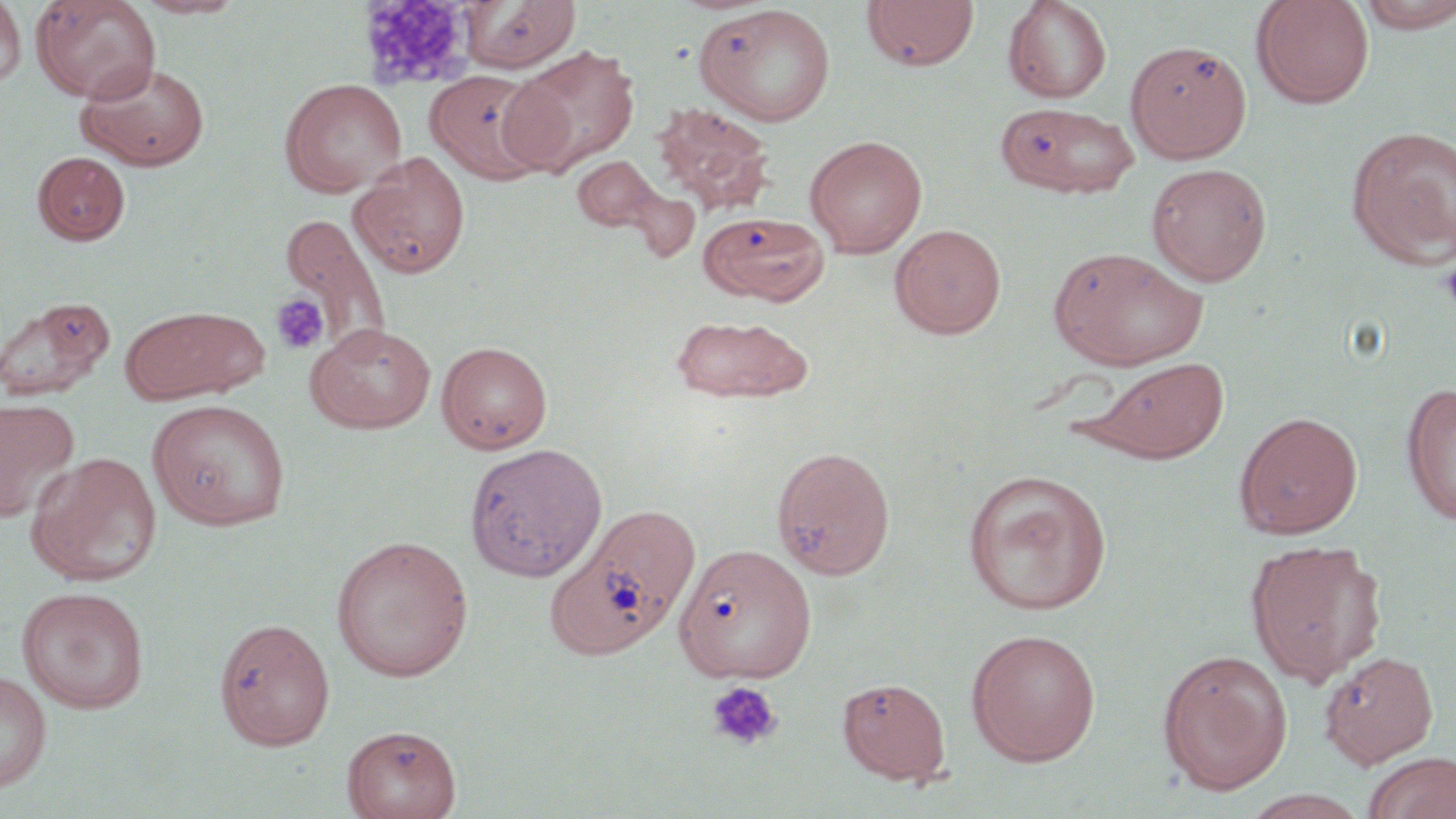

Summary:
  - Coordinate format: approximate bounding boxes as (x1,y1)-(x2,y2) corner pairs in pixels
  - Platelet locations: (1439,257)-(1456,313), (271,293)-(329,355), (706,681)-(783,750)
  - White blood cell locations: (355,1)-(482,92)
  - Uninfected red blood cell locations: (30,0)-(162,103), (133,0)-(247,19), (460,0)-(581,72), (861,0)-(980,72), (1003,0)-(1112,103), (1250,0)-(1376,109), (0,1)-(27,89), (1355,1)-(1456,32), (694,4)-(837,127), (1125,41)-(1252,163), (504,46)-(639,175), (75,58)-(211,171), (425,69)-(551,184), (495,71)-(582,176), (279,78)-(407,197), (995,101)-(1140,198), (653,102)-(775,215), (1346,125)-(1456,268), (804,134)-(928,257), (32,151)-(130,245), (349,151)-(471,279), (572,156)-(662,234), (1146,162)-(1272,286), (627,188)-(700,262), (697,213)-(831,305), (274,215)-(391,359), (889,224)-(1006,339), (1048,245)-(1208,370), (0,295)-(115,402), (121,305)-(267,403), (669,313)-(813,403), (304,321)-(437,434), (436,341)-(553,453), (1079,356)-(1230,463), (1400,381)-(1456,526), (0,397)-(80,521), (147,399)-(291,530), (1234,411)-(1363,539), (464,442)-(608,583), (771,445)-(896,580), (25,451)-(162,587), (961,469)-(1112,615), (545,504)-(701,661), (331,534)-(474,682), (1245,539)-(1386,687), (677,544)-(816,684), (16,586)-(150,714), (214,617)-(336,751), (966,628)-(1101,765), (1156,648)-(1293,795), (1319,650)-(1439,767), (0,671)-(52,793), (837,677)-(951,784), (342,724)-(461,819), (1361,752)-(1456,819), (1240,790)-(1370,818)
  - Slide-level diagnosis: no evidence of blood parasites
  - Stain: May-Grünwald-Giemsa
  - Image size: 1456×819 pixels
  - Field of view: one of a larger specimen
  - Magnification: 1000x
  - Modality: optical microscopy
  - Preparation: thin blood smear